Assess for parasitized red blood cells.
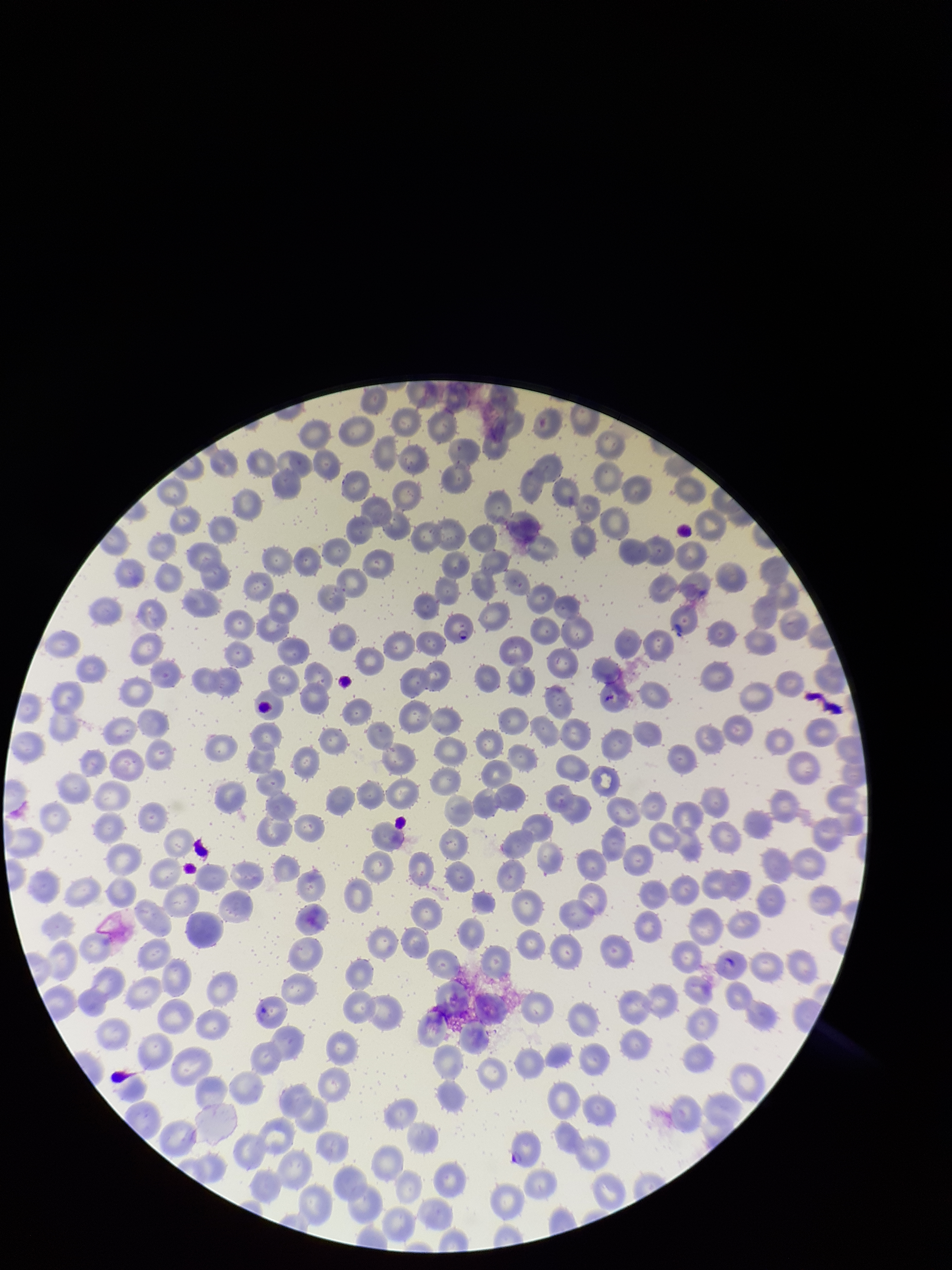
Seen.

parasitized red blood cell count = 1
species reported for this patient = Plasmodium falciparum
image size = 952×1270 pixels
preparation = thin blood smear
capture = smartphone photograph through the microscope eyepiece
field of view = one from this slide
patient malaria status = infected
stain = Giemsa
red blood cell count = 264